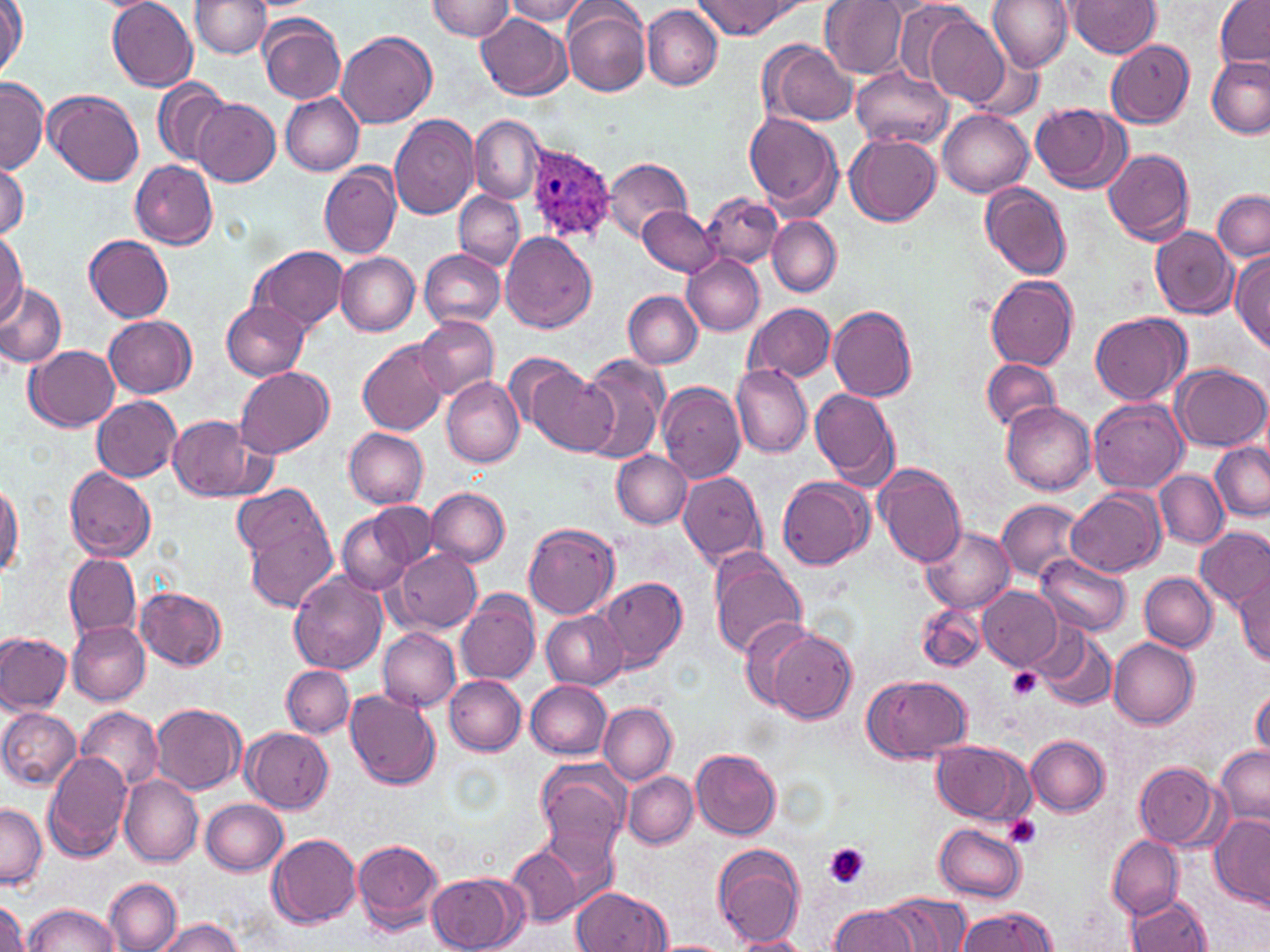

Approximate bounding boxes as (x1,y1)-(x2,y2) corner pairs in pixels. Uninfected red blood cell locations: (107,0)-(198,92), (192,0)-(272,56), (428,0)-(514,40), (504,0)-(590,24), (820,0)-(909,78), (986,0)-(1072,71), (1066,0)-(1161,58), (1214,0)-(1269,67), (695,1)-(797,38), (0,2)-(26,78), (563,4)-(651,98), (642,5)-(723,90), (916,12)-(1011,108), (260,13)-(348,105), (477,13)-(572,100), (337,30)-(437,129), (1106,39)-(1195,128), (760,40)-(856,129), (968,53)-(1042,121), (1206,58)-(1270,139), (851,66)-(953,151), (0,78)-(48,174), (154,79)-(230,168), (46,89)-(144,186), (279,93)-(365,176), (192,99)-(280,187), (1030,102)-(1131,195), (937,110)-(1035,198), (745,111)-(844,217), (389,114)-(480,219), (469,115)-(544,204), (846,133)-(942,227), (1102,148)-(1196,246), (601,158)-(692,239), (130,160)-(217,249), (0,161)-(28,238), (319,162)-(402,259), (980,181)-(1071,281), (703,190)-(782,267), (1213,191)-(1269,262), (454,192)-(524,270), (638,204)-(722,277), (767,217)-(841,297), (1151,227)-(1237,319), (500,230)-(596,333), (0,231)-(27,321), (85,234)-(175,323), (249,245)-(350,334), (419,249)-(506,328), (1230,250)-(1270,352), (334,251)-(421,335), (683,254)-(765,336), (986,275)-(1078,370), (0,282)-(67,368), (622,291)-(702,369), (222,301)-(308,379), (743,302)-(835,384), (828,304)-(917,402), (1091,313)-(1191,406), (105,315)-(197,398), (415,315)-(499,401), (358,339)-(449,436), (25,346)-(119,431), (503,353)-(597,448), (575,353)-(671,465), (980,358)-(1061,433), (731,364)-(811,458), (1171,364)-(1268,451), (234,366)-(335,458), (441,376)-(524,467), (656,382)-(747,482), (809,387)-(899,488), (92,396)-(182,481), (1089,398)-(1186,492), (1002,401)-(1097,494), (170,415)-(259,500), (343,427)-(429,510), (1210,443)-(1270,521), (612,450)-(691,529), (874,465)-(968,569), (63,466)-(156,562), (1155,470)-(1227,548), (677,471)-(767,568), (778,476)-(874,570), (0,480)-(22,579), (232,484)-(329,561), (426,487)-(510,567), (1067,490)-(1163,578), (998,499)-(1085,580), (367,502)-(436,570), (338,511)-(417,596), (245,516)-(338,612), (523,524)-(621,618), (919,525)-(1015,614), (1195,525)-(1270,612), (709,547)-(808,658), (393,549)-(481,634), (63,553)-(142,642), (1037,555)-(1130,636), (1233,571)-(1270,665), (289,572)-(388,674), (1140,573)-(1218,651), (598,576)-(688,674), (978,586)-(1062,670), (135,587)-(227,669), (455,589)-(541,686), (917,604)-(986,673), (540,610)-(627,690), (738,618)-(818,706), (66,621)-(149,705), (379,628)-(460,711), (768,629)-(857,723), (1034,630)-(1118,712), (0,633)-(70,714), (1108,637)-(1199,729), (282,666)-(354,738), (862,673)-(972,763), (445,676)-(526,754), (524,680)-(612,758), (1250,688)-(1269,762), (345,690)-(441,790), (599,702)-(677,784), (151,703)-(246,797), (78,705)-(164,793), (0,707)-(81,790), (241,727)-(335,813), (1025,734)-(1110,816), (931,739)-(1035,826), (1216,744)-(1269,824), (691,748)-(782,840), (42,749)-(134,862), (536,757)-(631,860), (1134,761)-(1226,850), (623,771)-(698,848), (119,775)-(204,866), (200,798)-(288,875), (0,803)-(47,890), (1208,818)-(1270,908), (541,822)-(622,911), (935,823)-(1026,901), (267,833)-(360,928), (1107,836)-(1183,917), (352,839)-(443,933), (712,844)-(805,947), (506,846)-(580,928), (426,871)-(525,952), (103,878)-(181,952), (572,887)-(670,952), (880,891)-(969,951), (1127,894)-(1212,951), (1,899)-(31,952), (23,902)-(120,952), (829,907)-(919,952), (957,908)-(1058,952), (154,918)-(247,952), (729,935)-(813,952). Plasmodium ovale-infected red blood cell locations: (524,142)-(615,244). Platelet locations: (1006,667)-(1043,703), (1003,816)-(1041,849), (823,843)-(868,887). Slide-level diagnosis: Plasmodium ovale. May-Grünwald-Giemsa-stained preparation. Captured at 1000x magnification. Image is 1270×952 pixels. Optical microscopy. Thin blood smear. Single field of view.